Identify the preparation type.
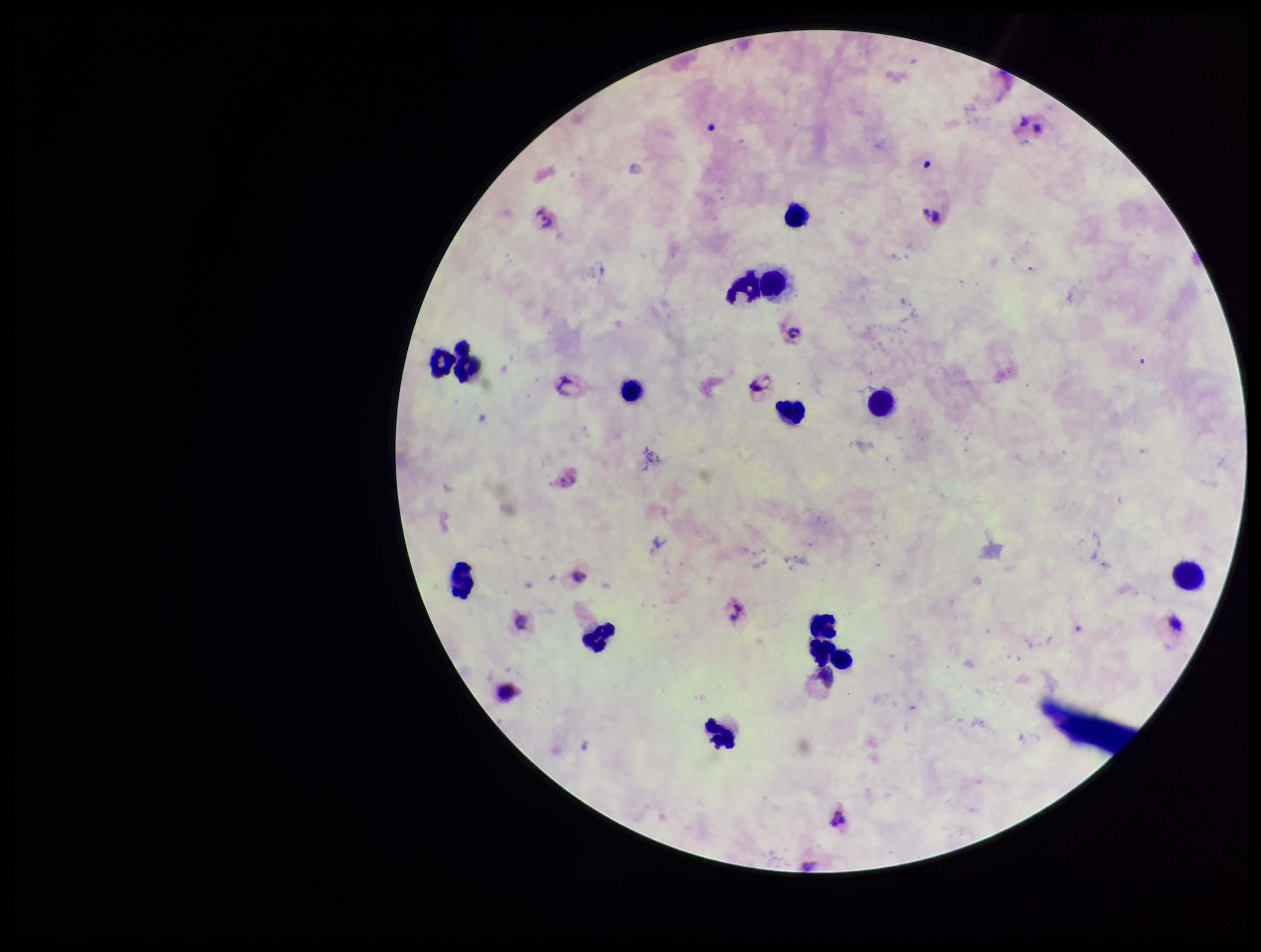
A thick smear.

Leukocyte count: 12. Photographed through the microscope eyepiece with a smartphone camera. Giemsa stain. One field from this slide. Species reported for this patient: Plasmodium vivax. Patient malaria status: infected. Parasite count: 0. Image is 1261×952 pixels. Plasmodium parasites: none identified.